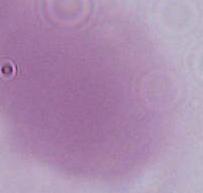 An erythrocyte is seen. Micrograph. Captured at 1000x magnification.